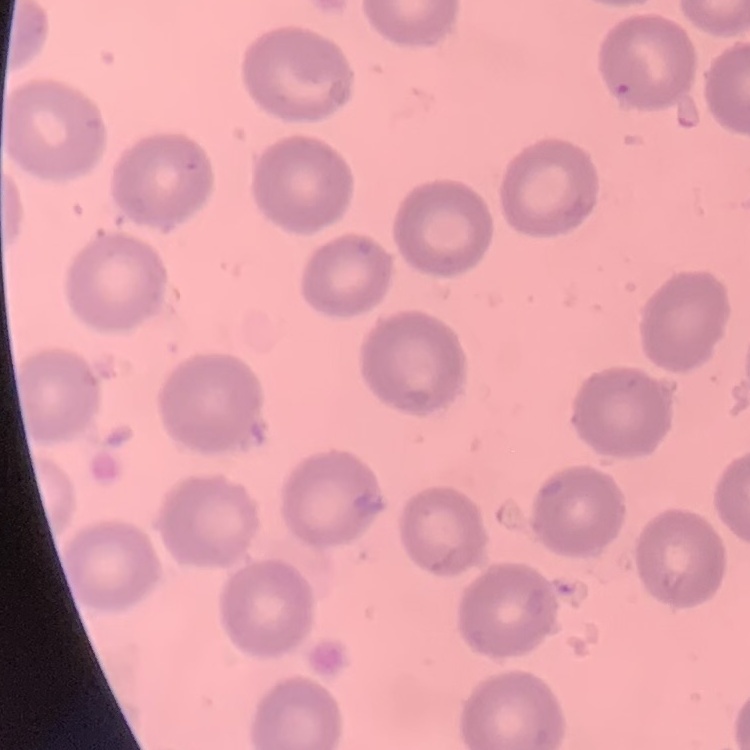 The erythrocytes show no rouleaux formation. One tile cut from a larger photomicrograph. Stained with either Field's or Giemsa. Thin peripheral smear.